Assess the morphology of the red blood cells.
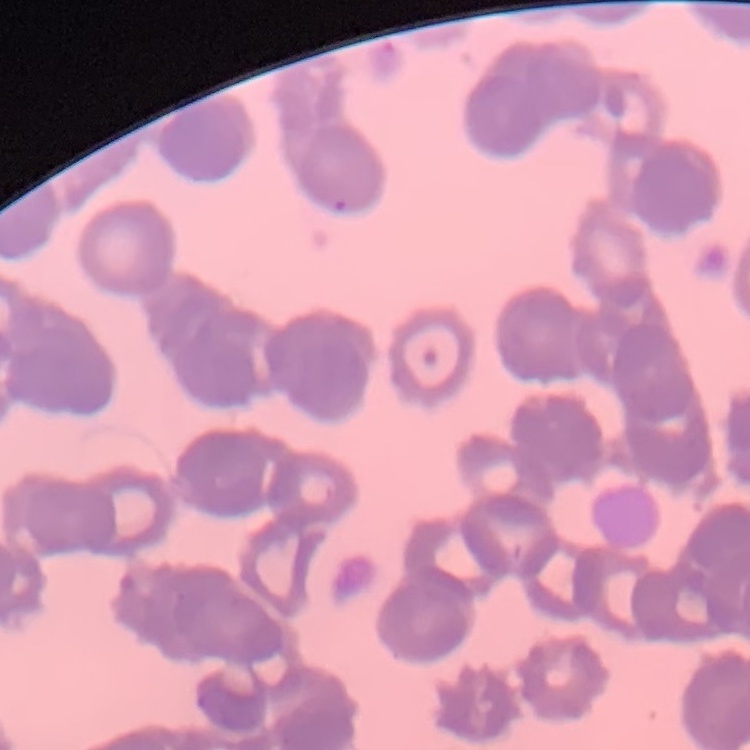

They show rouleaux formation.

{
  "preparation": "thin peripheral smear",
  "image_type": "one tile cut from a larger photomicrograph",
  "stain": "Field's or Giemsa"
}